Report the malaria status of this cell.
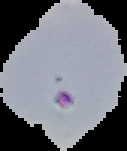
Parasitized.

{
  "preparation": "thin blood smear",
  "image_size": "127×151 pixels",
  "image_type": "segmented cell region on a black background"
}